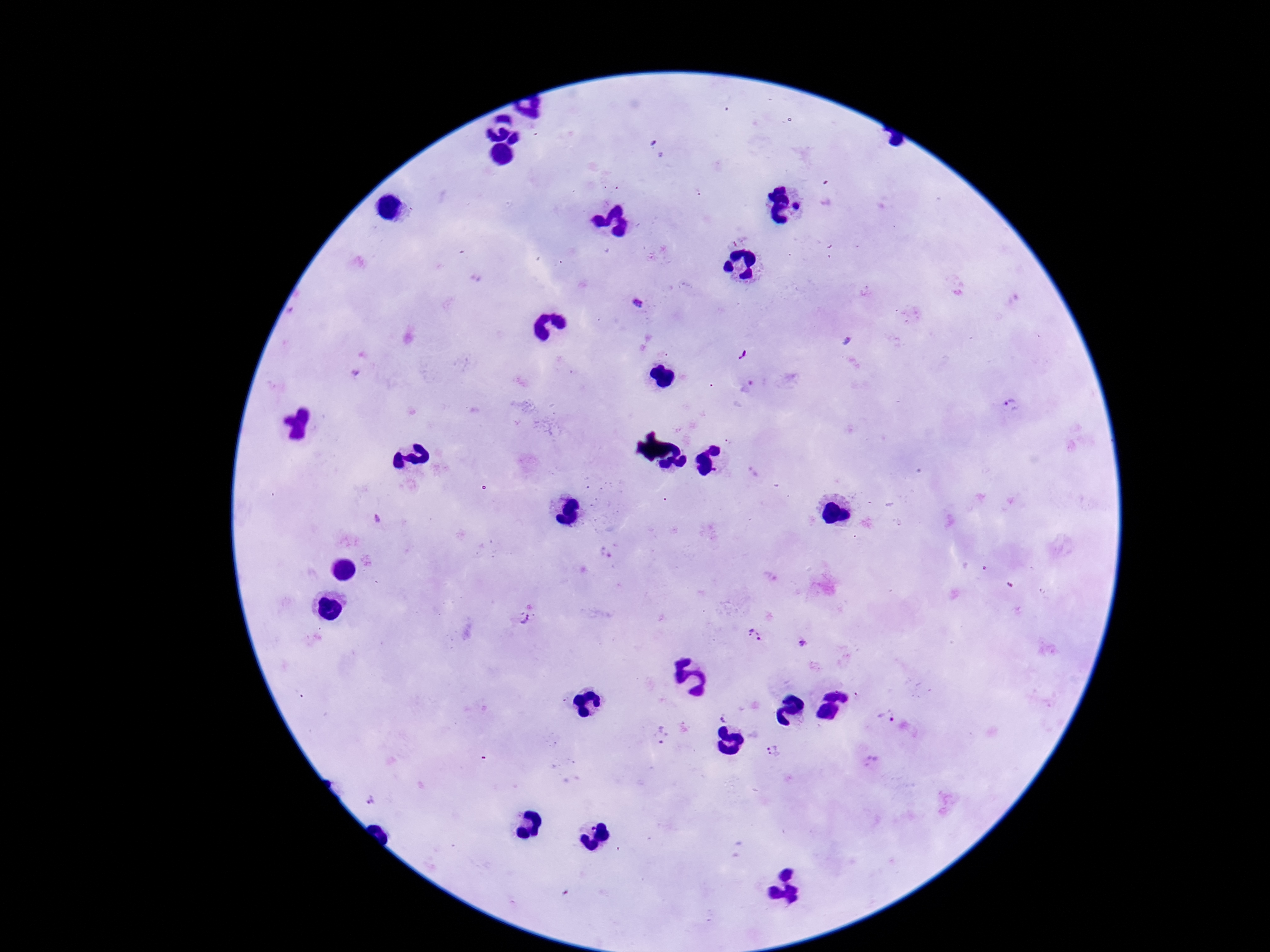

Approximate centers as {x, y} in pixels. Plasmodium parasite locations: {637, 303}, {743, 356}, {1011, 406}, {729, 441}, {378, 521}, {526, 618}, {755, 635}, {803, 643}, {887, 716}, {724, 717}, {662, 737}, {773, 751}, {872, 762}, {370, 798}. Giemsa stain. 100x magnification. Image is 1270×952 pixels. One field from this slide. Smartphone photograph taken through the microscope eyepiece. Patient malaria status: infected. Thick blood film.